Give the position of each P. falciparum parasite with its life-cycle stage, each leukocyte, and any debris.
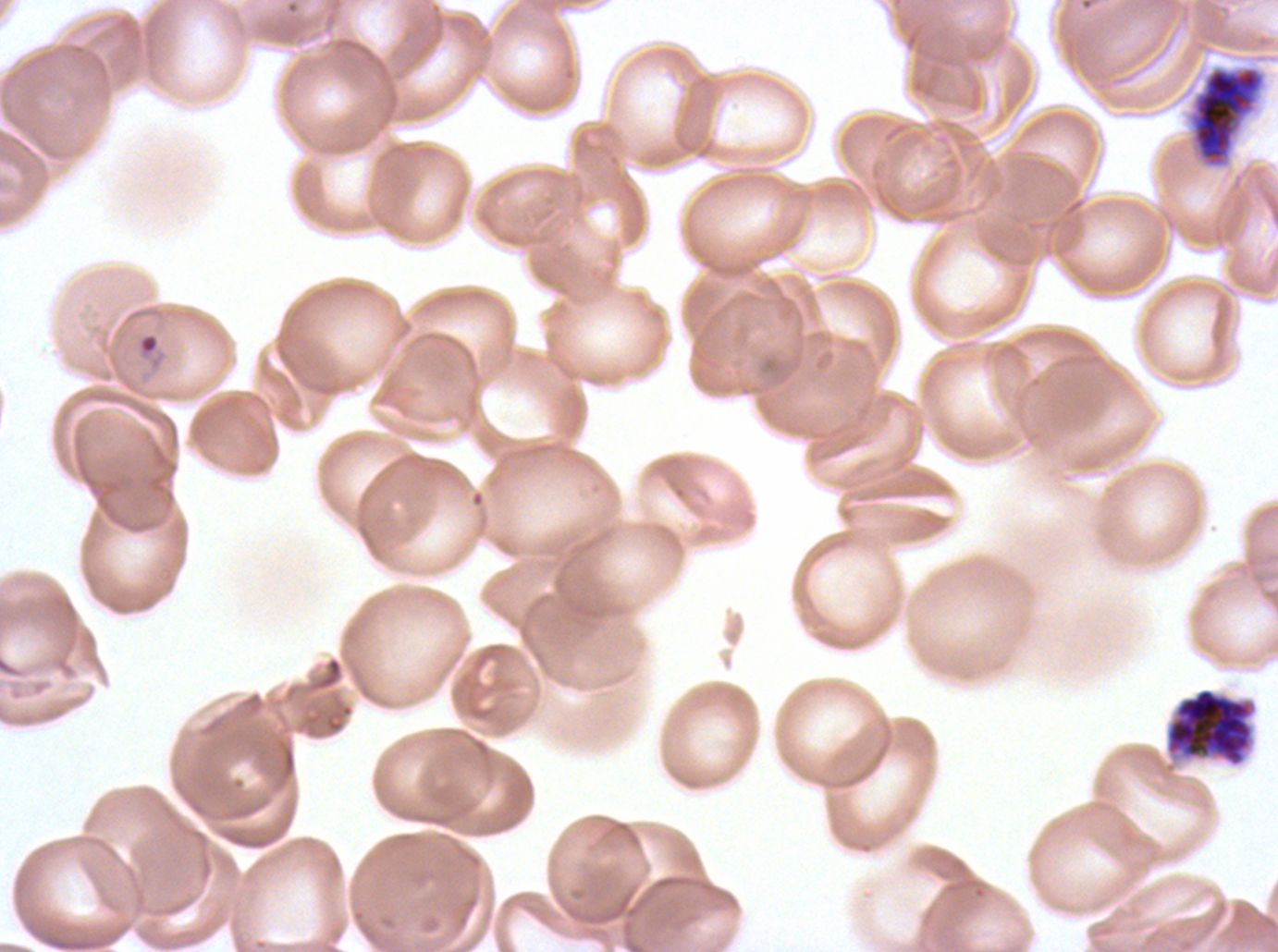

Approximate bounding boxes as {x1, y1, x2, y2} in pixels.
Rings: {133, 330, 169, 384}.
Late schizonts: {1189, 66, 1265, 168}, {1166, 688, 1254, 766}.
No late-ring/early-trophozoite forms, mid trophozoites, late trophozoites, early schizonts, segmenters, gametocytes, leukocytes, or debris observed.

specimen = P. falciparum cultured ex vivo for 24 to 48 hours, from a patient in The Gambia
stain = Giemsa
life-cycle stages observed = ring, late schizont
preparation = thin blood film
image size = 1278×952 pixels
field of view = sub-image separated from a larger composite